Outline each blood parasite and name the species.
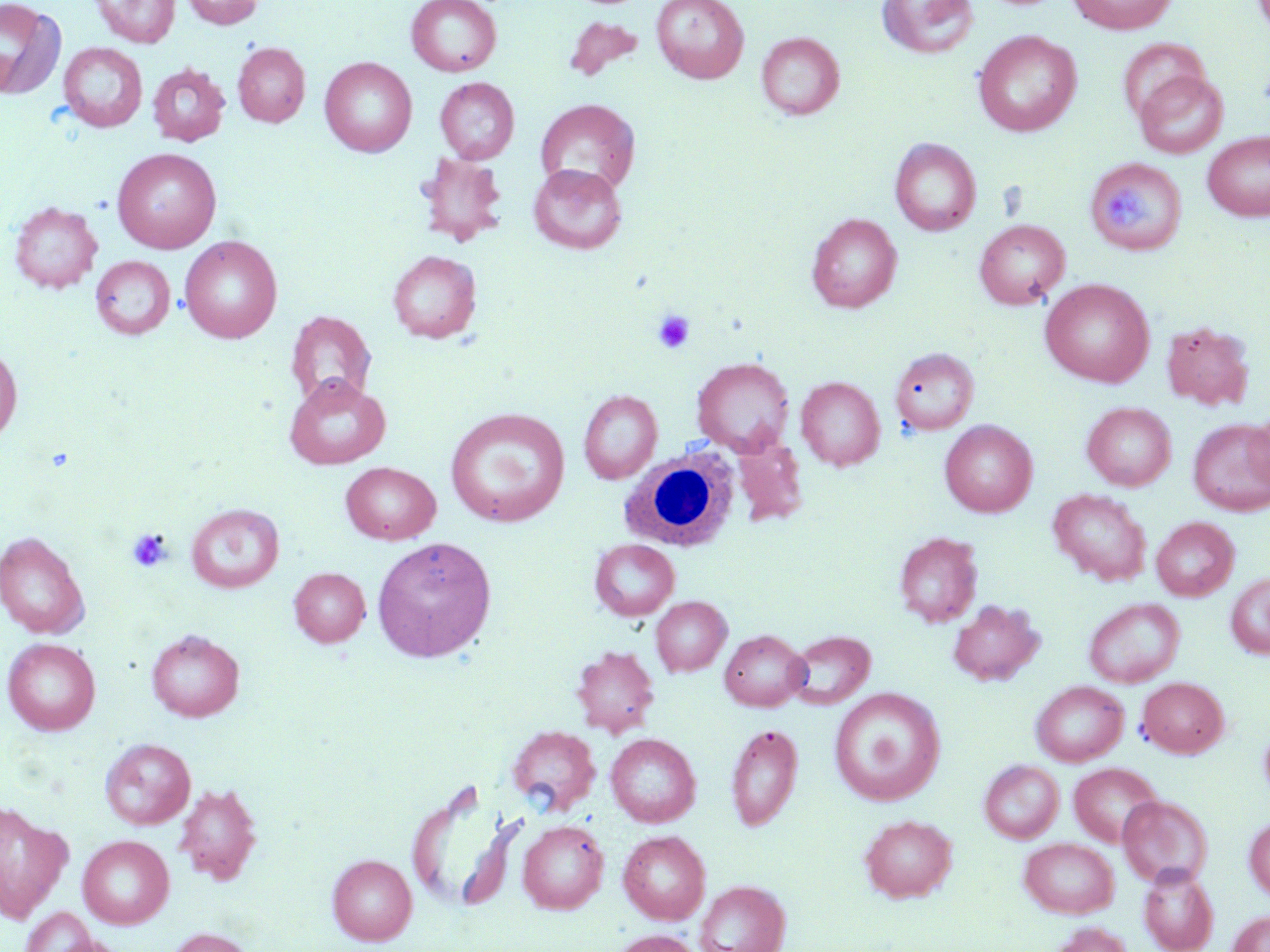

No blood parasites observed.

Summary:
  - Coordinate format: approximate bounding boxes as [x1, y1, x2, y2] in pixels
  - White blood cell locations: [618, 444, 739, 552]
  - Platelet locations: [1110, 189, 1148, 230], [652, 310, 696, 354], [127, 527, 173, 572]
  - Uninfected red blood cell locations: [90, 0, 180, 48], [181, 0, 264, 29], [406, 0, 502, 76], [652, 0, 749, 83], [876, 0, 980, 59], [1066, 0, 1179, 34], [0, 1, 67, 101], [564, 16, 644, 82], [972, 30, 1081, 137], [756, 32, 845, 119], [1117, 37, 1212, 126], [58, 42, 148, 132], [232, 42, 310, 127], [320, 57, 417, 157], [147, 64, 229, 146], [1133, 69, 1229, 159], [435, 77, 519, 164], [535, 98, 641, 195], [1202, 132, 1270, 221], [890, 137, 981, 236], [112, 148, 222, 253], [415, 153, 509, 246], [1091, 163, 1191, 256], [528, 164, 627, 254], [9, 200, 102, 293], [806, 213, 902, 312], [973, 219, 1070, 309], [180, 236, 283, 343], [387, 250, 481, 343], [90, 255, 176, 339], [1040, 278, 1155, 387], [286, 310, 376, 407], [1161, 320, 1255, 411], [0, 343, 22, 444], [891, 346, 980, 437], [691, 357, 795, 455], [284, 375, 390, 470], [796, 376, 885, 470], [578, 389, 662, 483], [1082, 402, 1177, 491], [445, 408, 571, 527], [1246, 409, 1270, 496], [1188, 418, 1270, 515], [940, 420, 1037, 517], [731, 435, 808, 527], [341, 462, 441, 544], [1048, 488, 1151, 586], [186, 503, 285, 593], [1152, 517, 1239, 601], [0, 531, 89, 639], [894, 532, 983, 627], [372, 536, 496, 663], [589, 539, 679, 621], [289, 567, 369, 647], [1226, 573, 1270, 659], [651, 596, 731, 676], [1083, 597, 1185, 688], [947, 599, 1045, 686], [146, 629, 244, 721], [719, 630, 809, 711], [785, 630, 875, 709], [2, 637, 101, 735], [572, 645, 659, 737], [1137, 677, 1229, 758], [1031, 680, 1128, 766], [829, 688, 945, 805], [725, 722, 803, 832], [506, 725, 600, 814], [1258, 725, 1270, 801], [605, 733, 701, 827], [100, 738, 195, 829], [980, 760, 1064, 843], [1069, 762, 1163, 847], [405, 781, 513, 913], [174, 782, 262, 885], [1117, 795, 1213, 888], [0, 803, 71, 923], [859, 814, 957, 902], [1245, 817, 1270, 900], [517, 819, 608, 913], [618, 830, 711, 924], [77, 834, 174, 929], [1019, 838, 1119, 918], [327, 854, 416, 945], [1139, 866, 1219, 952], [695, 880, 790, 952], [18, 907, 99, 951], [1228, 910, 1270, 952], [1048, 921, 1133, 952], [163, 927, 257, 952], [610, 929, 703, 952], [47, 935, 133, 952]
  - Slide-level diagnosis: negative for blood parasites
  - Magnification: 1000x
  - Stain: May-Grünwald-Giemsa
  - Modality: light microscopy
  - Image size: 1270×952 pixels
  - Preparation: thin blood smear
  - Field of view: single